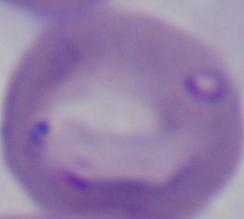
modality = micrograph
identification = Babesia
magnification = 1000x